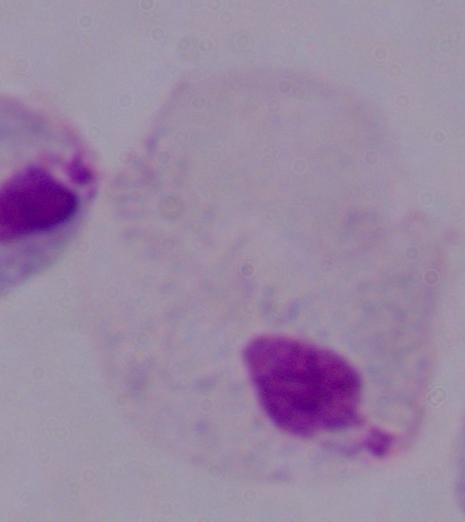

Summary:
  - Identification: trichomonad
  - Magnification: 1000x
  - Modality: micrograph